Give the extent of all uninfected red blood cells.
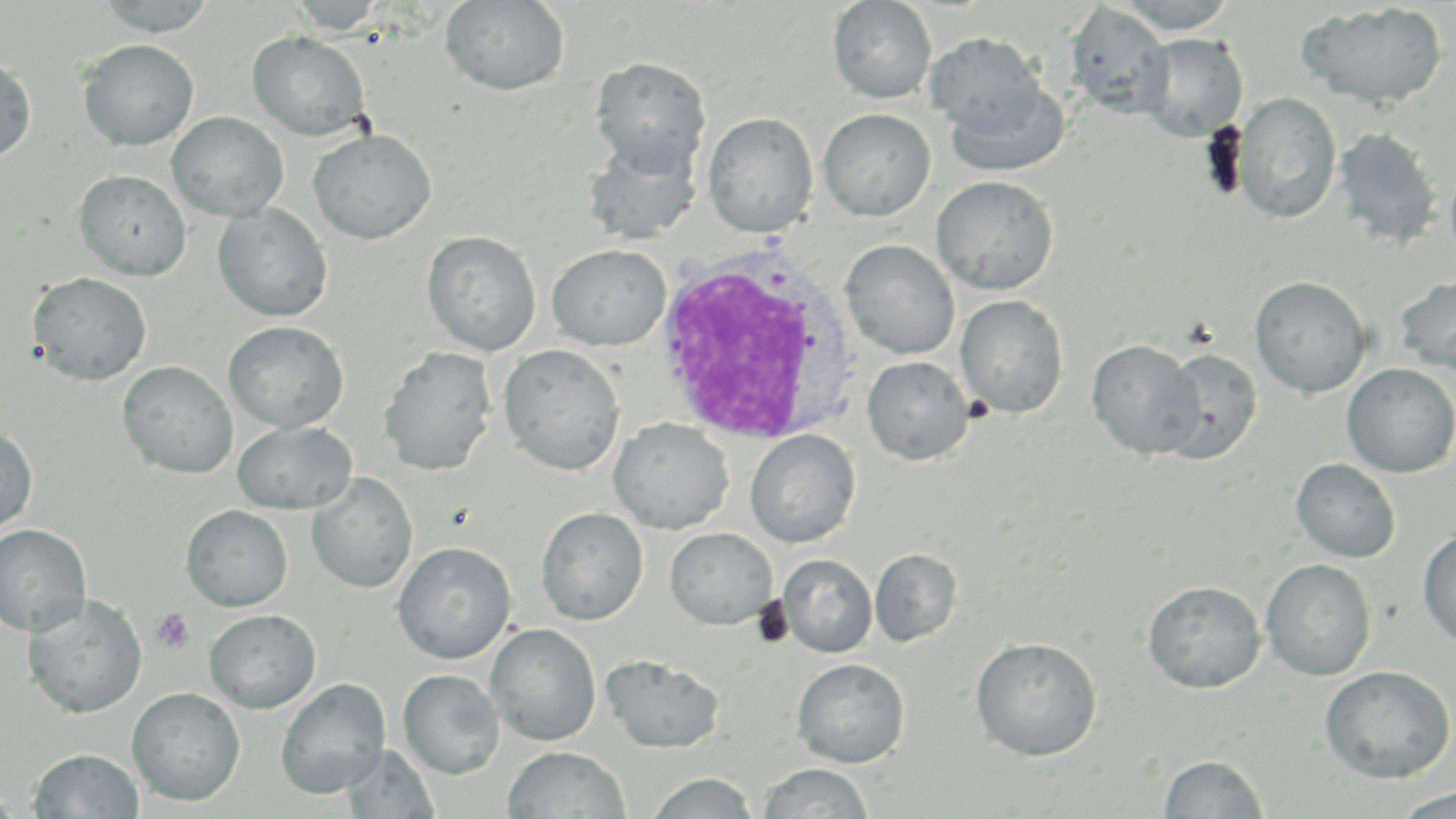
Approximate bounding boxes as named x1/y1/x2/y2 corners in pixels.
Uninfected red blood cells: (x1=95, y1=0, x2=218, y2=36), (x1=288, y1=0, x2=388, y2=36), (x1=828, y1=0, x2=937, y2=104), (x1=1114, y1=0, x2=1239, y2=34), (x1=440, y1=1, x2=571, y2=97), (x1=1296, y1=2, x2=1448, y2=111), (x1=1064, y1=3, x2=1173, y2=118), (x1=247, y1=31, x2=371, y2=141), (x1=925, y1=32, x2=1045, y2=134), (x1=1137, y1=33, x2=1248, y2=142), (x1=78, y1=39, x2=199, y2=150), (x1=0, y1=52, x2=36, y2=164), (x1=590, y1=57, x2=711, y2=174), (x1=944, y1=77, x2=1071, y2=178), (x1=1233, y1=92, x2=1342, y2=224), (x1=818, y1=108, x2=936, y2=221), (x1=167, y1=111, x2=289, y2=221), (x1=703, y1=112, x2=818, y2=237), (x1=1331, y1=127, x2=1443, y2=250), (x1=309, y1=130, x2=436, y2=244), (x1=583, y1=136, x2=702, y2=245), (x1=1444, y1=159, x2=1456, y2=269), (x1=74, y1=170, x2=191, y2=280), (x1=932, y1=175, x2=1059, y2=295), (x1=214, y1=203, x2=333, y2=322), (x1=422, y1=231, x2=541, y2=356), (x1=841, y1=240, x2=959, y2=360), (x1=547, y1=244, x2=671, y2=350), (x1=1394, y1=272, x2=1456, y2=376), (x1=28, y1=273, x2=152, y2=385), (x1=1250, y1=276, x2=1372, y2=397), (x1=955, y1=294, x2=1069, y2=419), (x1=224, y1=321, x2=349, y2=433), (x1=1087, y1=339, x2=1205, y2=459), (x1=499, y1=344, x2=625, y2=474), (x1=379, y1=347, x2=497, y2=476), (x1=1157, y1=348, x2=1262, y2=464), (x1=862, y1=356, x2=974, y2=465), (x1=118, y1=361, x2=237, y2=478), (x1=1341, y1=363, x2=1456, y2=478), (x1=609, y1=418, x2=734, y2=535), (x1=233, y1=420, x2=356, y2=514), (x1=0, y1=426, x2=38, y2=536), (x1=745, y1=429, x2=860, y2=548), (x1=1291, y1=458, x2=1401, y2=563), (x1=306, y1=472, x2=418, y2=593), (x1=181, y1=505, x2=293, y2=611), (x1=536, y1=507, x2=648, y2=625), (x1=0, y1=524, x2=92, y2=637), (x1=1417, y1=526, x2=1456, y2=649), (x1=666, y1=528, x2=777, y2=629), (x1=393, y1=542, x2=516, y2=664), (x1=871, y1=548, x2=962, y2=647), (x1=777, y1=554, x2=877, y2=658), (x1=1260, y1=559, x2=1376, y2=680), (x1=1143, y1=580, x2=1266, y2=693), (x1=24, y1=594, x2=147, y2=718), (x1=204, y1=610, x2=321, y2=713), (x1=486, y1=623, x2=601, y2=746), (x1=970, y1=637, x2=1103, y2=761), (x1=602, y1=654, x2=725, y2=754), (x1=792, y1=658, x2=910, y2=768), (x1=1319, y1=665, x2=1455, y2=783), (x1=399, y1=669, x2=504, y2=779), (x1=276, y1=679, x2=390, y2=799), (x1=128, y1=688, x2=245, y2=806), (x1=340, y1=744, x2=441, y2=818), (x1=503, y1=746, x2=630, y2=819), (x1=30, y1=749, x2=144, y2=818), (x1=1159, y1=754, x2=1269, y2=817), (x1=757, y1=763, x2=873, y2=819), (x1=647, y1=771, x2=760, y2=818), (x1=0, y1=784, x2=18, y2=818), (x1=1390, y1=788, x2=1456, y2=818).

Summary:
  - White blood cell locations: (x1=649, y1=245, x2=864, y2=447)
  - Platelet locations: (x1=150, y1=607, x2=194, y2=653)
  - Slide-level diagnosis: Plasmodium ovale
  - Field of view: single
  - Stain: May-Grünwald-Giemsa
  - Modality: optical microscopy
  - Image size: 1456×819 pixels
  - Magnification: 1000x
  - Preparation: thin blood smear